Locate malaria parasites and leukocytes.
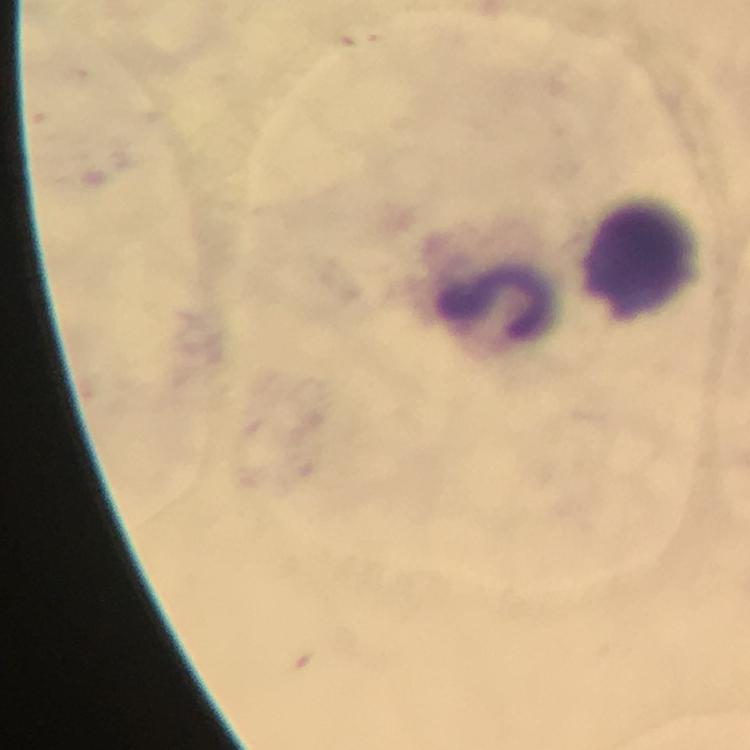

No malaria parasites detected.
Approximate centers as {x, y} in pixels.
Leukocytes: {644, 255}, {500, 304}.

capture: smartphone camera through the microscope
preparation: thick smear
image_size: 750×750 pixels
context: from a diagnostic examination for malaria
cropped_from: a single field of view
magnification: 100x
stain: Giemsa
immersion_oil: applied